Give the extent of all uninfected red blood cells.
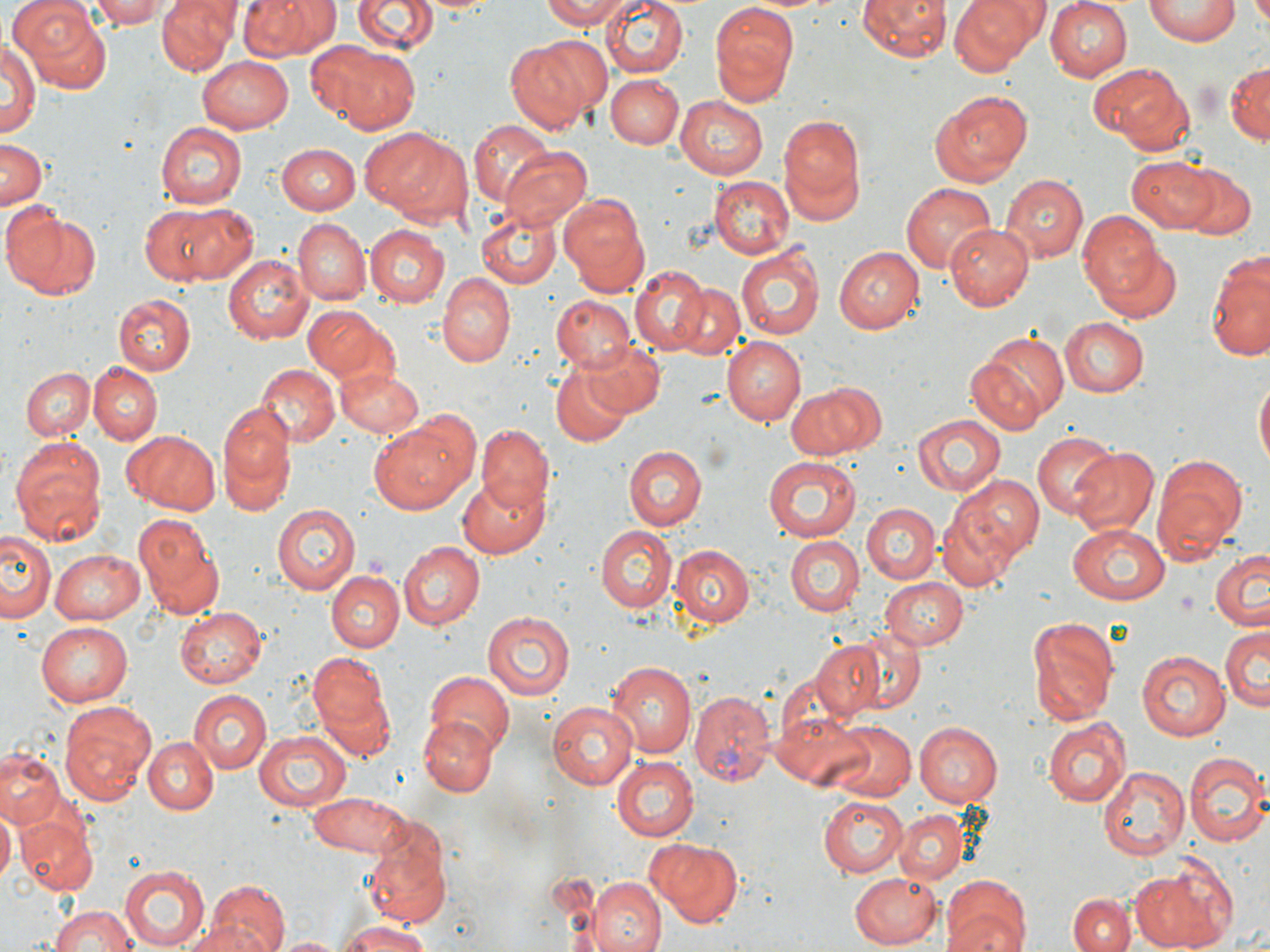
Approximate bounding boxes as [x1, y1, x2, y2] in pixels.
Uninfected red blood cells: [11, 0, 114, 92], [86, 0, 172, 29], [157, 0, 238, 76], [237, 0, 338, 62], [353, 0, 436, 55], [415, 0, 498, 16], [538, 0, 637, 28], [600, 0, 687, 78], [858, 0, 949, 63], [949, 0, 1045, 74], [1043, 0, 1133, 82], [1146, 1, 1240, 45], [1249, 1, 1270, 38], [709, 2, 798, 104], [1, 35, 39, 142], [504, 40, 595, 134], [326, 46, 423, 135], [198, 55, 294, 131], [1225, 61, 1268, 147], [1088, 63, 1193, 153], [605, 75, 682, 149], [930, 90, 1034, 186], [675, 95, 768, 179], [776, 112, 865, 221], [468, 120, 557, 211], [155, 122, 245, 210], [359, 127, 466, 223], [0, 135, 48, 208], [279, 143, 360, 213], [499, 146, 592, 231], [1127, 155, 1219, 232], [1175, 164, 1258, 242], [1000, 173, 1087, 265], [709, 175, 794, 260], [901, 182, 996, 275], [560, 192, 650, 293], [4, 204, 102, 300], [141, 204, 249, 286], [475, 205, 561, 290], [1074, 212, 1165, 305], [292, 218, 368, 306], [945, 222, 1034, 309], [363, 225, 449, 307], [1092, 242, 1183, 324], [736, 245, 822, 341], [834, 246, 923, 334], [1207, 249, 1270, 361], [223, 255, 311, 344], [630, 267, 710, 353], [436, 273, 516, 367], [670, 283, 745, 362], [114, 293, 194, 376], [551, 295, 634, 372], [303, 306, 395, 386], [1060, 317, 1149, 396], [724, 336, 806, 424], [582, 338, 666, 419], [967, 351, 1057, 436], [86, 363, 160, 444], [255, 364, 337, 447], [334, 365, 423, 440], [553, 366, 631, 448], [21, 367, 93, 440], [1254, 376, 1269, 476], [785, 383, 878, 459], [217, 405, 296, 511], [911, 414, 1007, 496], [368, 417, 474, 515], [475, 425, 554, 515], [121, 429, 222, 513], [1031, 432, 1115, 519], [8, 435, 111, 546], [625, 445, 707, 529], [610, 446, 694, 608], [1069, 447, 1159, 536], [1151, 453, 1246, 565], [764, 457, 860, 541], [953, 473, 1044, 561], [456, 475, 547, 560], [861, 501, 939, 584], [273, 502, 361, 595], [936, 502, 1023, 592], [134, 510, 224, 617], [1065, 523, 1168, 604], [595, 524, 677, 611], [3, 529, 56, 625], [786, 535, 863, 616], [399, 542, 485, 630], [669, 542, 756, 633], [49, 549, 145, 625], [1209, 549, 1269, 632], [328, 569, 403, 652], [880, 577, 969, 649], [176, 607, 266, 688], [483, 610, 576, 700], [1027, 616, 1117, 726], [37, 622, 134, 708], [839, 626, 928, 715], [1220, 627, 1268, 713], [810, 639, 885, 719], [1137, 649, 1231, 740], [310, 653, 388, 731], [607, 658, 698, 757], [423, 669, 514, 756], [314, 681, 397, 765], [187, 690, 270, 774], [58, 702, 156, 807], [547, 702, 638, 790], [773, 710, 874, 789], [420, 717, 495, 795], [1043, 717, 1131, 808], [827, 721, 915, 801], [914, 721, 1004, 805], [252, 730, 350, 811], [143, 736, 219, 813], [0, 749, 64, 827], [1183, 751, 1267, 846], [612, 757, 698, 841], [1097, 767, 1188, 861], [305, 790, 415, 857], [817, 796, 908, 876], [0, 805, 17, 880], [894, 810, 967, 885], [17, 813, 96, 896], [360, 820, 455, 925], [646, 838, 744, 925], [1131, 861, 1232, 950], [117, 865, 211, 950], [849, 873, 940, 948], [940, 875, 1031, 952], [587, 877, 665, 952], [206, 882, 289, 952], [1068, 893, 1134, 952], [45, 902, 137, 952], [338, 919, 437, 952], [178, 922, 270, 952], [274, 935, 346, 952].

slide_level_diagnosis: Plasmodium vivax
magnification: 1000x
field_of_view: one of a larger specimen
plasmodium_vivax_infected_red_blood_cell_locations: 'approximate bounding boxes as [x1, y1, x2, y2] in pixels: [689, 689, 774, 785]'
preparation: thin blood film
stain: May-Grünwald-Giemsa
modality: light microscopy
image_size: 1270×952 pixels